Report the malaria status.
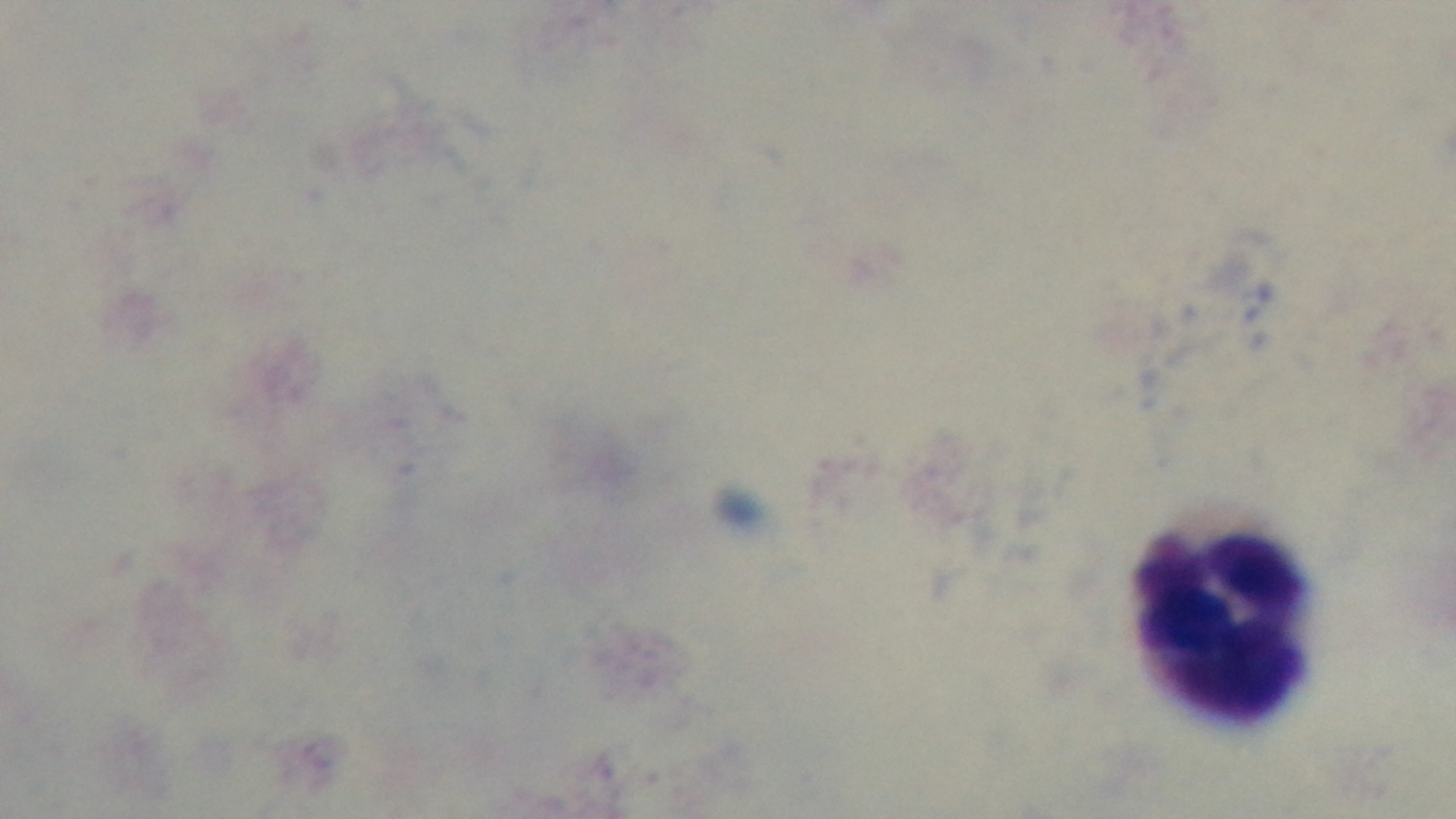

Negative.

Giemsa-stained. Light microscopy. Preparation: thick smear. Captured with a mounted 4K digital camera. Single field of view. Oil-immersion objective, 100x.